Evaluate for parasitized red blood cells.
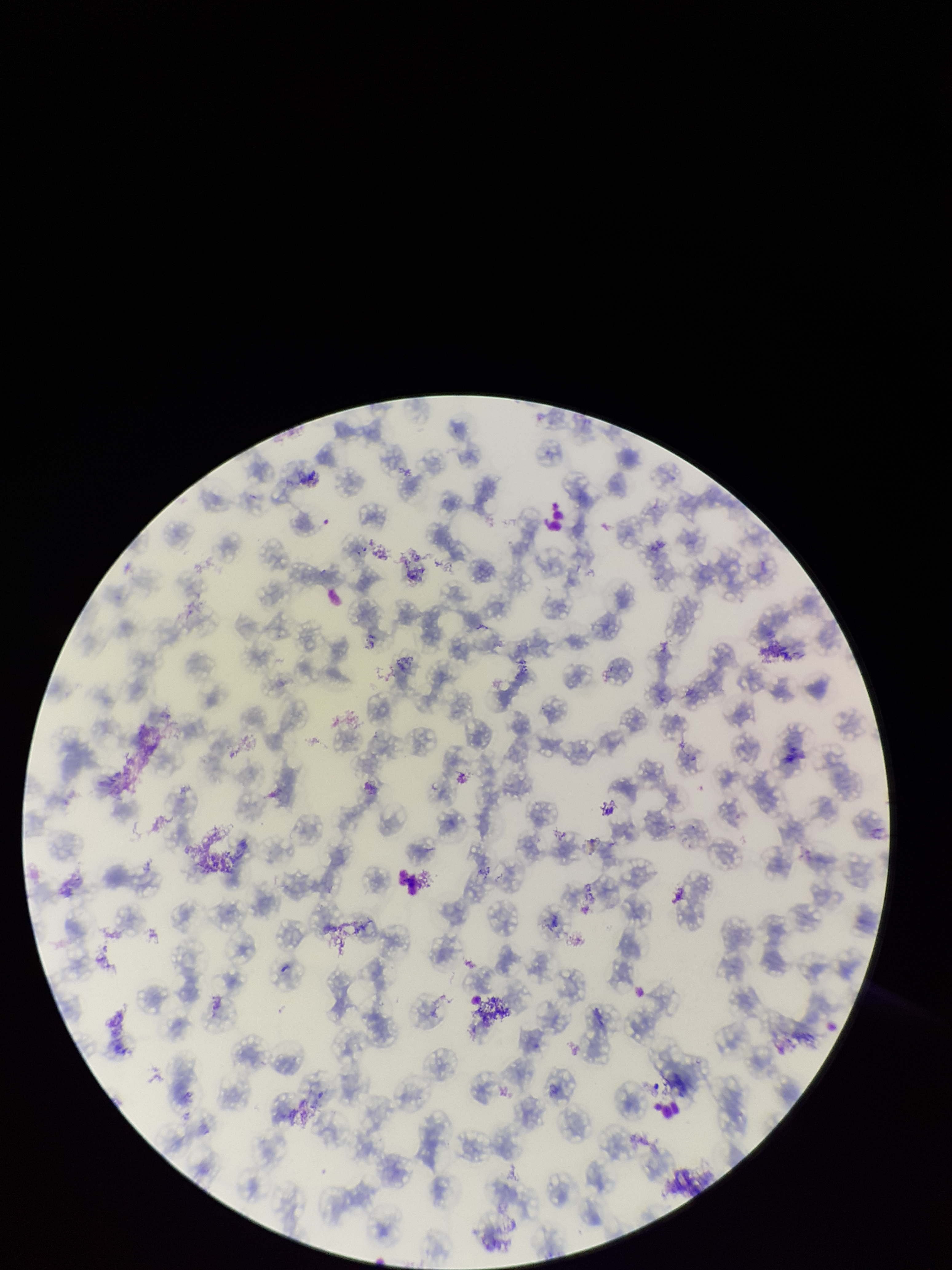

None identified.

stain = Giemsa
field of view = one from this slide
patient malaria status = infected
preparation = thin
capture = smartphone photograph through the microscope eyepiece
parasitized red blood cell count = 0
species reported for this patient = Plasmodium falciparum
image size = 952×1270 pixels
red blood cell count = 161